Report the malaria status of this cell.
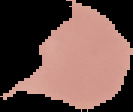

It is uninfected.

Summary:
  - Image type: cell region segmented out of the field of view; surrounding area masked to black
  - Image size: 133×112 pixels
  - Preparation: thin blood film